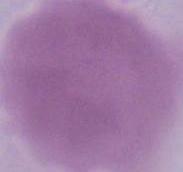

{
  "identification": "red blood cell",
  "magnification": "1000x",
  "modality": "photomicrograph"
}